Identify the parasite.
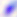

Toxoplasma gondii.

modality = photomicrograph
magnification = 400x